Classify this cell by malaria status.
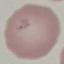
It is uninfected.

stain = Giemsa
capture = smartphone through the microscope eyepiece
preparation = thin blood film
image type = automatically extracted cell patch, resized to 64 × 64 pixels